State the blood parasite species.
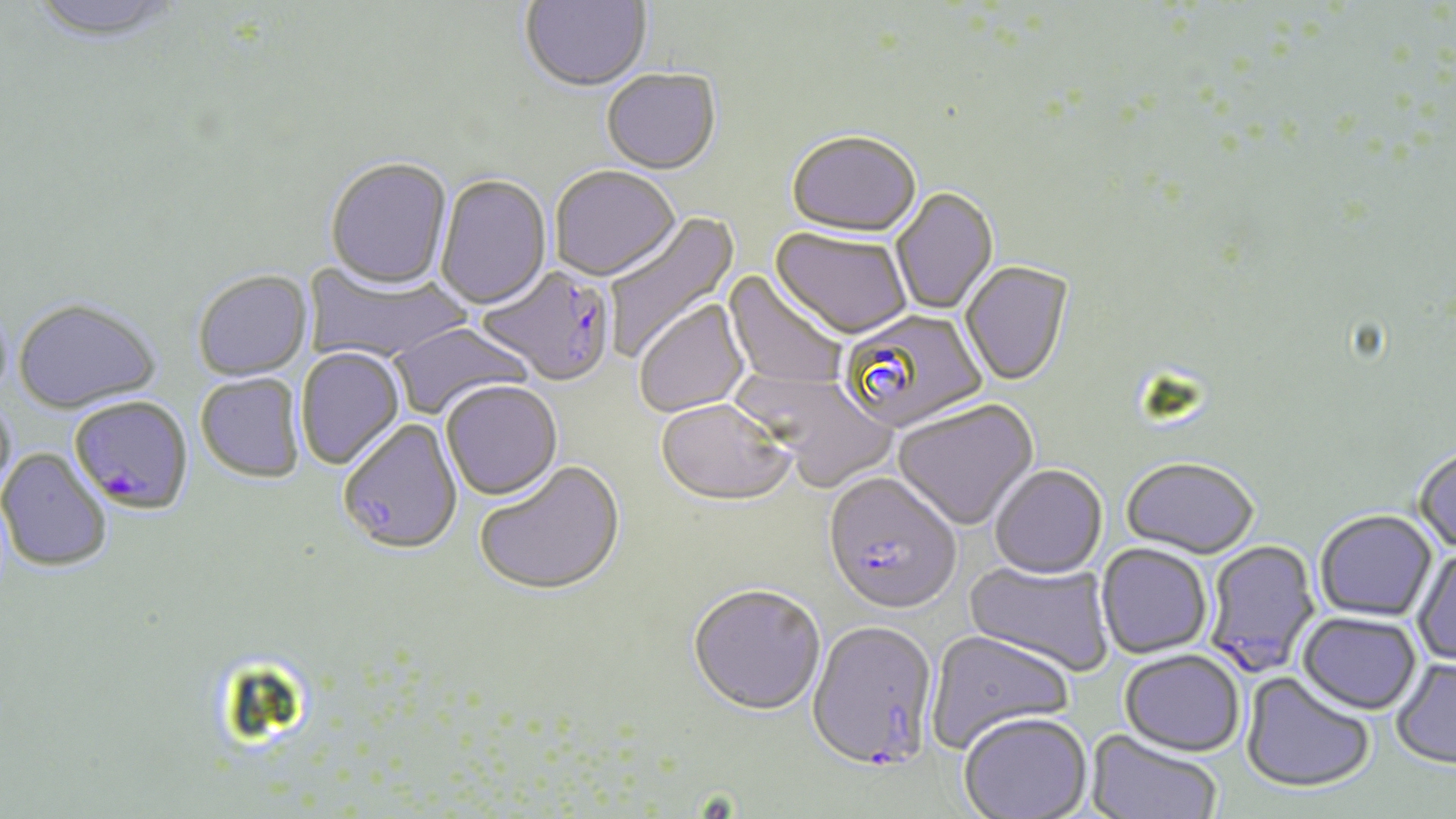
Plasmodium falciparum.

magnification = 1000x
stain = May-Grünwald-Giemsa
modality = optical microscopy
image size = 1456×819 pixels
field of view = single
uninfected red blood cell locations = approximate bounding boxes as (x1,y1)-(x2,y2) corner pairs in pixels: (23,0)-(186,45), (520,0)-(652,94), (601,71)-(722,177), (785,134)-(921,241), (325,160)-(453,292), (550,167)-(680,284), (435,176)-(553,312), (892,188)-(999,316), (603,211)-(740,360), (770,230)-(912,342), (302,261)-(471,365), (960,262)-(1074,388), (723,270)-(847,390), (193,272)-(313,382), (13,299)-(161,415), (634,300)-(750,418), (388,322)-(535,421), (296,348)-(406,471), (739,370)-(899,493), (196,374)-(305,484), (440,382)-(563,503), (0,396)-(17,504), (655,399)-(796,508), (893,400)-(1039,532), (338,419)-(463,556), (0,448)-(112,573), (1413,448)-(1456,555), (1121,460)-(1260,561), (474,461)-(625,598), (989,467)-(1108,581), (1315,511)-(1437,622), (1095,544)-(1212,660), (1411,546)-(1456,668), (963,558)-(1115,678), (688,586)-(827,717), (1298,613)-(1422,716), (926,631)-(1075,753), (1119,651)-(1245,758), (1390,657)-(1456,770), (1240,672)-(1376,795), (958,715)-(1093,819), (1086,730)-(1222,819)
preparation = thin blood film
Plasmodium falciparum-infected red blood cell locations = approximate bounding boxes as (x1,y1)-(x2,y2) corner pairs in pixels: (476,265)-(617,388), (840,310)-(987,435), (72,395)-(193,519), (823,476)-(962,618), (1201,539)-(1320,678), (807,621)-(938,771)